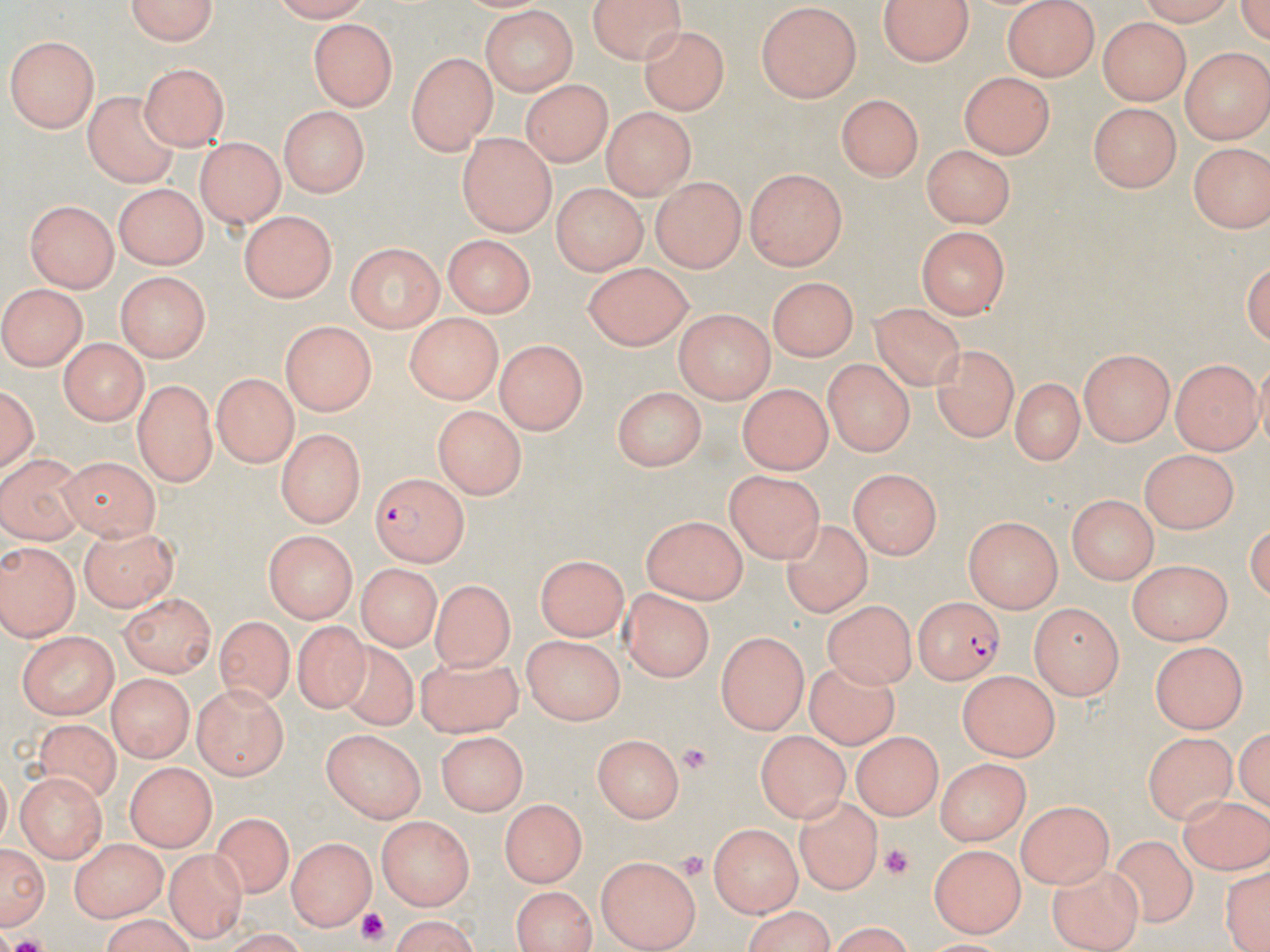

Approximate bounding boxes as named x1/y1/x2/y2 corners in pixels. Plasmodium falciparum-infected red blood cell locations: (x1=370, y1=474, x2=468, y2=566), (x1=913, y1=598, x2=1003, y2=687). Platelet locations: (x1=680, y1=743, x2=715, y2=772), (x1=881, y1=843, x2=912, y2=880), (x1=678, y1=848, x2=708, y2=882), (x1=354, y1=909, x2=390, y2=944). Uninfected red blood cell locations: (x1=584, y1=0, x2=691, y2=62), (x1=1126, y1=0, x2=1239, y2=24), (x1=116, y1=1, x2=220, y2=48), (x1=881, y1=1, x2=973, y2=66), (x1=1002, y1=1, x2=1102, y2=80), (x1=755, y1=4, x2=862, y2=103), (x1=478, y1=8, x2=579, y2=94), (x1=1100, y1=18, x2=1190, y2=103), (x1=309, y1=19, x2=397, y2=110), (x1=641, y1=26, x2=727, y2=112), (x1=7, y1=35, x2=102, y2=132), (x1=1180, y1=48, x2=1270, y2=140), (x1=407, y1=52, x2=494, y2=155), (x1=141, y1=61, x2=226, y2=149), (x1=959, y1=70, x2=1057, y2=156), (x1=522, y1=78, x2=611, y2=166), (x1=82, y1=88, x2=184, y2=188), (x1=837, y1=94, x2=925, y2=181), (x1=1089, y1=102, x2=1183, y2=189), (x1=278, y1=104, x2=367, y2=198), (x1=602, y1=108, x2=693, y2=199), (x1=457, y1=133, x2=555, y2=234), (x1=197, y1=137, x2=285, y2=230), (x1=1186, y1=139, x2=1268, y2=233), (x1=923, y1=144, x2=1017, y2=226), (x1=744, y1=167, x2=849, y2=270), (x1=652, y1=177, x2=746, y2=270), (x1=113, y1=183, x2=208, y2=269), (x1=551, y1=183, x2=644, y2=274), (x1=25, y1=199, x2=117, y2=291), (x1=239, y1=210, x2=334, y2=300), (x1=915, y1=226, x2=1006, y2=318), (x1=443, y1=237, x2=533, y2=319), (x1=346, y1=242, x2=444, y2=330), (x1=582, y1=260, x2=692, y2=351), (x1=114, y1=271, x2=211, y2=364), (x1=770, y1=275, x2=858, y2=361), (x1=4, y1=282, x2=89, y2=372), (x1=862, y1=300, x2=974, y2=394), (x1=674, y1=310, x2=773, y2=402), (x1=405, y1=314, x2=499, y2=403), (x1=278, y1=322, x2=372, y2=415), (x1=58, y1=337, x2=150, y2=423), (x1=497, y1=340, x2=588, y2=433), (x1=931, y1=342, x2=1018, y2=439), (x1=1079, y1=350, x2=1175, y2=446), (x1=1171, y1=357, x2=1259, y2=453), (x1=823, y1=359, x2=912, y2=457), (x1=212, y1=371, x2=300, y2=465), (x1=1013, y1=377, x2=1084, y2=462), (x1=1, y1=382, x2=38, y2=482), (x1=131, y1=383, x2=216, y2=486), (x1=737, y1=384, x2=835, y2=472), (x1=609, y1=385, x2=706, y2=469), (x1=433, y1=404, x2=526, y2=497), (x1=278, y1=428, x2=363, y2=523), (x1=1139, y1=449, x2=1241, y2=536), (x1=0, y1=450, x2=85, y2=544), (x1=58, y1=456, x2=164, y2=539), (x1=727, y1=466, x2=827, y2=565), (x1=847, y1=467, x2=942, y2=563), (x1=1067, y1=493, x2=1158, y2=583), (x1=640, y1=513, x2=746, y2=604), (x1=964, y1=515, x2=1065, y2=612), (x1=780, y1=519, x2=876, y2=621), (x1=78, y1=525, x2=181, y2=611), (x1=263, y1=530, x2=355, y2=621), (x1=0, y1=542, x2=76, y2=641), (x1=536, y1=554, x2=625, y2=641), (x1=1129, y1=561, x2=1232, y2=646), (x1=354, y1=567, x2=438, y2=652), (x1=431, y1=581, x2=520, y2=667), (x1=622, y1=587, x2=710, y2=680), (x1=121, y1=590, x2=215, y2=677), (x1=825, y1=602, x2=916, y2=689), (x1=1030, y1=605, x2=1124, y2=702), (x1=217, y1=618, x2=297, y2=700), (x1=294, y1=618, x2=375, y2=713), (x1=717, y1=631, x2=808, y2=734), (x1=13, y1=632, x2=117, y2=718), (x1=522, y1=634, x2=623, y2=725), (x1=329, y1=639, x2=418, y2=728), (x1=1150, y1=639, x2=1244, y2=732), (x1=419, y1=658, x2=528, y2=737), (x1=800, y1=659, x2=902, y2=748), (x1=956, y1=669, x2=1061, y2=757), (x1=106, y1=674, x2=194, y2=761), (x1=195, y1=683, x2=289, y2=778), (x1=36, y1=718, x2=127, y2=804), (x1=321, y1=730, x2=426, y2=825), (x1=439, y1=730, x2=524, y2=815), (x1=754, y1=731, x2=852, y2=818), (x1=1146, y1=733, x2=1235, y2=822), (x1=850, y1=734, x2=943, y2=818), (x1=591, y1=735, x2=683, y2=823), (x1=937, y1=759, x2=1030, y2=843), (x1=127, y1=763, x2=213, y2=850), (x1=14, y1=773, x2=105, y2=863), (x1=1181, y1=794, x2=1269, y2=874), (x1=796, y1=795, x2=879, y2=893), (x1=497, y1=800, x2=588, y2=886), (x1=1017, y1=801, x2=1115, y2=889), (x1=206, y1=812, x2=297, y2=901), (x1=378, y1=816, x2=474, y2=911), (x1=707, y1=821, x2=803, y2=916), (x1=288, y1=832, x2=372, y2=928), (x1=1106, y1=833, x2=1202, y2=928), (x1=0, y1=837, x2=49, y2=935), (x1=69, y1=839, x2=166, y2=920), (x1=928, y1=841, x2=1027, y2=933), (x1=167, y1=851, x2=243, y2=938), (x1=593, y1=856, x2=702, y2=950), (x1=1050, y1=860, x2=1146, y2=952), (x1=1218, y1=862, x2=1270, y2=952), (x1=511, y1=886, x2=597, y2=952), (x1=95, y1=914, x2=198, y2=952), (x1=384, y1=917, x2=486, y2=950). Slide-level diagnosis: Plasmodium falciparum. Optical microscopy. 1000x magnification. May-Grünwald-Giemsa-stained preparation. One field of a larger specimen. Image is 1270×952 pixels. Thin blood smear.